Locate every Plasmodium malariae-infected red blood cell.
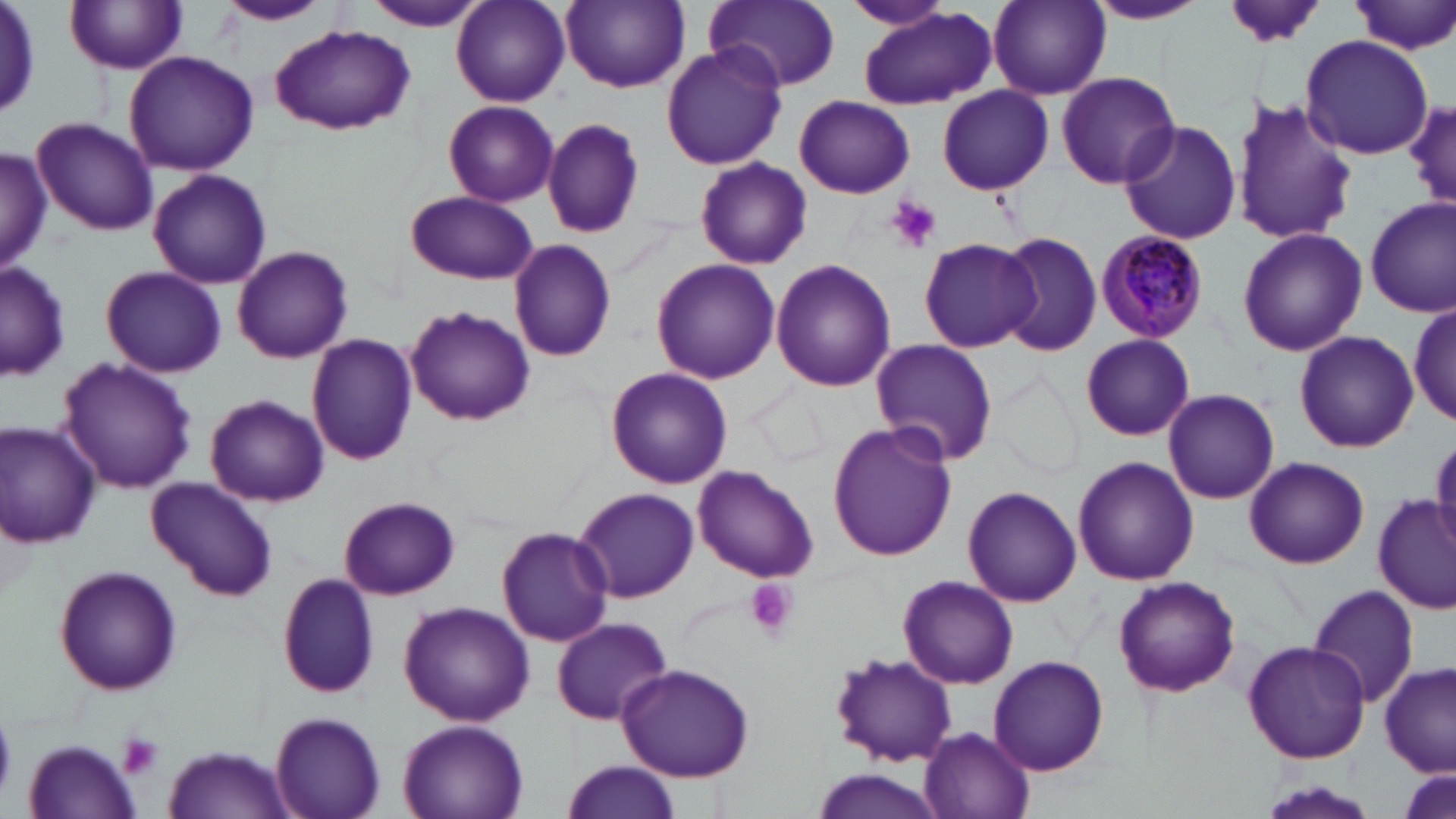
Approximate bounding boxes as [x1, y1, x2, y2] in pixels.
Plasmodium malariae-infected red blood cells: [1094, 230, 1210, 344].

slide_level_diagnosis: Plasmodium malariae
magnification: 1000x
field_of_view: single
platelet_locations: 'approximate bounding boxes as [x1, y1, x2, y2] in pixels: [888, 197, 942, 252], [742, 578, 799, 641], [0, 715, 17, 798], [117, 733, 164, 780]'
stain: May-Grünwald-Giemsa
image_size: 1456×819 pixels
preparation: thin blood smear
uninfected_red_blood_cell_locations: 'approximate bounding boxes as [x1, y1, x2, y2] in pixels: [1, 0, 42, 119], [212, 0, 334, 26], [450, 0, 569, 107], [561, 0, 689, 92], [1084, 0, 1208, 25], [357, 1, 492, 31], [705, 1, 841, 93], [836, 1, 959, 31], [988, 1, 1109, 100], [1349, 1, 1456, 56], [67, 2, 190, 74], [1223, 2, 1330, 49], [858, 7, 997, 108], [270, 25, 414, 134], [1301, 34, 1432, 159], [660, 44, 788, 170], [123, 51, 260, 176], [1054, 69, 1181, 190], [936, 86, 1054, 194], [794, 96, 914, 198], [1232, 96, 1356, 248], [1406, 100, 1455, 214], [442, 101, 558, 205], [31, 116, 157, 237], [542, 117, 647, 240], [1116, 120, 1244, 246], [0, 147, 51, 273], [694, 157, 811, 270], [148, 168, 271, 289], [404, 191, 539, 285], [1366, 198, 1456, 316], [1236, 227, 1367, 357], [995, 232, 1101, 356], [918, 236, 1038, 354], [509, 239, 617, 361], [231, 244, 353, 364], [650, 258, 780, 385], [770, 259, 896, 392], [0, 261, 70, 384], [100, 265, 226, 378], [1411, 300, 1455, 424], [404, 305, 535, 425], [1294, 330, 1418, 452], [305, 332, 418, 467], [1079, 334, 1196, 441], [870, 338, 999, 466], [57, 356, 196, 495], [989, 366, 1086, 483], [605, 367, 733, 489], [751, 380, 834, 472], [1163, 389, 1280, 504], [204, 393, 329, 507], [1, 421, 103, 547], [827, 421, 956, 563], [1429, 435, 1456, 550], [1073, 456, 1200, 585], [1244, 456, 1368, 568], [693, 463, 819, 583], [146, 476, 279, 601], [573, 486, 700, 604], [962, 486, 1082, 608], [338, 495, 459, 599], [1373, 495, 1456, 612], [496, 527, 615, 646], [53, 565, 183, 697], [275, 570, 382, 701], [896, 574, 1019, 690], [1112, 575, 1240, 696], [1309, 585, 1421, 707], [397, 600, 535, 725], [551, 615, 674, 726], [1243, 639, 1371, 764], [828, 651, 957, 766], [989, 655, 1109, 775], [617, 663, 755, 783], [1380, 663, 1455, 775], [270, 712, 386, 819], [397, 718, 528, 819], [919, 725, 1036, 819], [22, 739, 142, 817], [162, 746, 295, 819], [559, 761, 683, 819], [811, 766, 946, 819], [1257, 780, 1381, 819]'
modality: light microscopy